Report the malaria status of this cell.
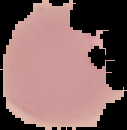
It is parasitized.

image size = 127×130 pixels
image type = segmented cell region with the area outside set to black
preparation = thin blood smear